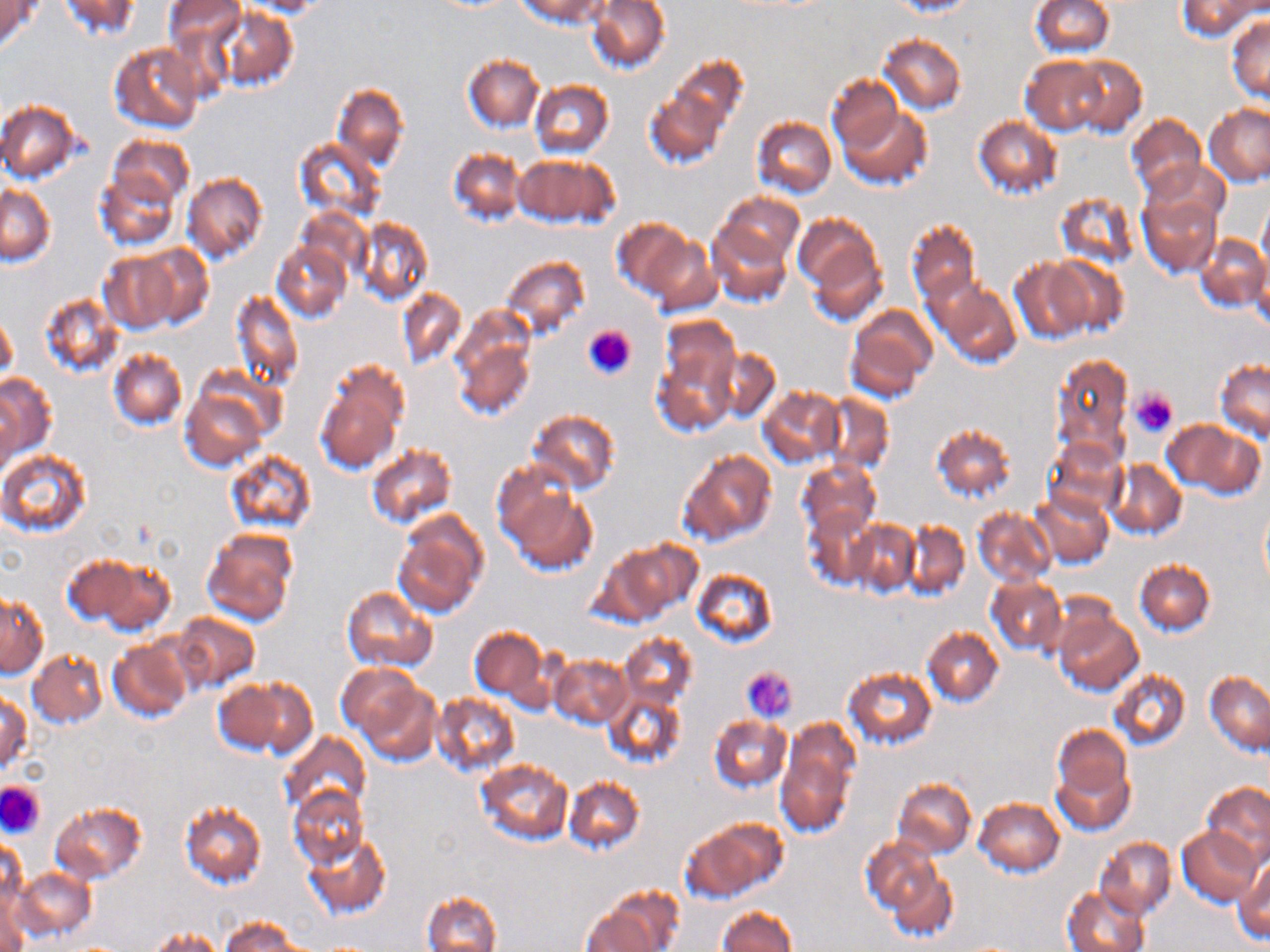

Summary:
  - Coordinate format: approximate bounding boxes as (x1, y1, x2, y2) in pixels
  - Uninfected red blood cell locations: (2, 0, 38, 52), (57, 0, 141, 40), (163, 0, 244, 52), (237, 0, 328, 16), (587, 0, 670, 74), (891, 0, 976, 16), (1030, 0, 1114, 57), (1178, 0, 1259, 41), (522, 1, 610, 29), (213, 7, 297, 91), (1226, 17, 1270, 103), (880, 33, 965, 113), (109, 42, 202, 135), (463, 54, 542, 130), (828, 54, 953, 140), (1021, 55, 1106, 134), (1065, 56, 1147, 137), (661, 59, 748, 152), (827, 75, 902, 152), (530, 81, 613, 158), (333, 84, 409, 171), (644, 85, 729, 170), (0, 99, 81, 183), (1204, 104, 1270, 185), (837, 105, 932, 189), (1126, 115, 1206, 200), (973, 116, 1062, 199), (753, 117, 836, 196), (106, 134, 194, 209), (294, 136, 384, 221), (448, 149, 526, 227), (514, 154, 617, 228), (1148, 157, 1230, 232), (95, 168, 180, 249), (182, 173, 268, 264), (0, 185, 55, 265), (1056, 191, 1140, 270), (715, 193, 803, 267), (1137, 194, 1220, 278), (1258, 197, 1270, 273), (296, 208, 369, 283), (793, 215, 883, 317), (354, 216, 433, 306), (612, 217, 694, 303), (706, 219, 792, 305), (906, 219, 980, 305), (1196, 234, 1270, 311), (644, 235, 721, 315), (272, 242, 350, 324), (132, 244, 213, 329), (100, 251, 179, 334), (499, 255, 591, 342), (1046, 256, 1129, 334), (1252, 257, 1269, 335), (1010, 258, 1090, 345), (933, 279, 1022, 368), (398, 287, 465, 370), (231, 290, 303, 390), (39, 293, 122, 376), (846, 308, 936, 400), (450, 310, 537, 421), (1, 315, 16, 381), (653, 316, 740, 437), (710, 347, 780, 423), (108, 348, 187, 430), (1052, 352, 1133, 461), (1215, 360, 1270, 442), (315, 361, 408, 474), (0, 375, 55, 459), (179, 386, 269, 469), (756, 386, 845, 467), (0, 392, 18, 482), (823, 392, 894, 474), (527, 408, 622, 496), (1162, 420, 1249, 493), (931, 422, 1015, 502), (1044, 438, 1127, 520), (365, 443, 457, 529), (0, 449, 91, 535), (678, 450, 776, 545), (227, 451, 315, 533), (796, 460, 880, 541), (1108, 460, 1186, 539), (499, 477, 597, 575), (1029, 489, 1113, 567), (1260, 503, 1270, 595), (973, 507, 1054, 588), (807, 508, 878, 588), (392, 510, 488, 618), (902, 519, 970, 601), (847, 520, 920, 594), (201, 527, 298, 626), (604, 536, 699, 622), (62, 554, 142, 627), (93, 559, 175, 636), (1136, 561, 1213, 635), (690, 567, 778, 649), (986, 574, 1066, 657), (342, 587, 437, 673), (1, 594, 47, 678), (1055, 611, 1142, 695), (172, 612, 260, 692), (468, 627, 548, 704), (923, 627, 1004, 707), (619, 632, 697, 712), (106, 639, 191, 723), (28, 650, 105, 728), (551, 655, 632, 730), (336, 664, 420, 738), (842, 667, 937, 750), (1108, 669, 1190, 751), (1205, 671, 1270, 756), (355, 674, 440, 766), (227, 676, 317, 757), (604, 689, 686, 769), (429, 692, 519, 777), (0, 693, 29, 774), (709, 715, 790, 793), (772, 723, 857, 839), (1052, 724, 1132, 807), (279, 732, 370, 822), (1051, 754, 1135, 837), (475, 758, 573, 845), (565, 777, 644, 854), (892, 779, 975, 858), (1202, 780, 1270, 865), (288, 786, 368, 869), (975, 798, 1064, 876), (180, 800, 266, 888), (50, 801, 147, 884), (684, 818, 785, 902), (1177, 826, 1262, 908), (302, 833, 392, 920), (862, 836, 941, 918), (1, 837, 26, 914), (1094, 837, 1176, 918), (1233, 857, 1270, 943), (886, 863, 959, 945), (12, 867, 96, 943), (0, 877, 28, 952), (1061, 886, 1150, 952), (422, 891, 501, 951), (581, 903, 668, 952), (717, 906, 797, 952), (219, 917, 305, 952), (147, 927, 226, 951)
  - Platelet locations: (582, 324, 636, 380), (1129, 389, 1178, 436), (743, 666, 797, 723), (0, 780, 45, 838)
  - Slide-level diagnosis: negative for blood parasites
  - Preparation: thin blood film
  - Field of view: single
  - Image size: 1270×952 pixels
  - Stain: May-Grünwald-Giemsa
  - Magnification: 1000x
  - Modality: light microscopy